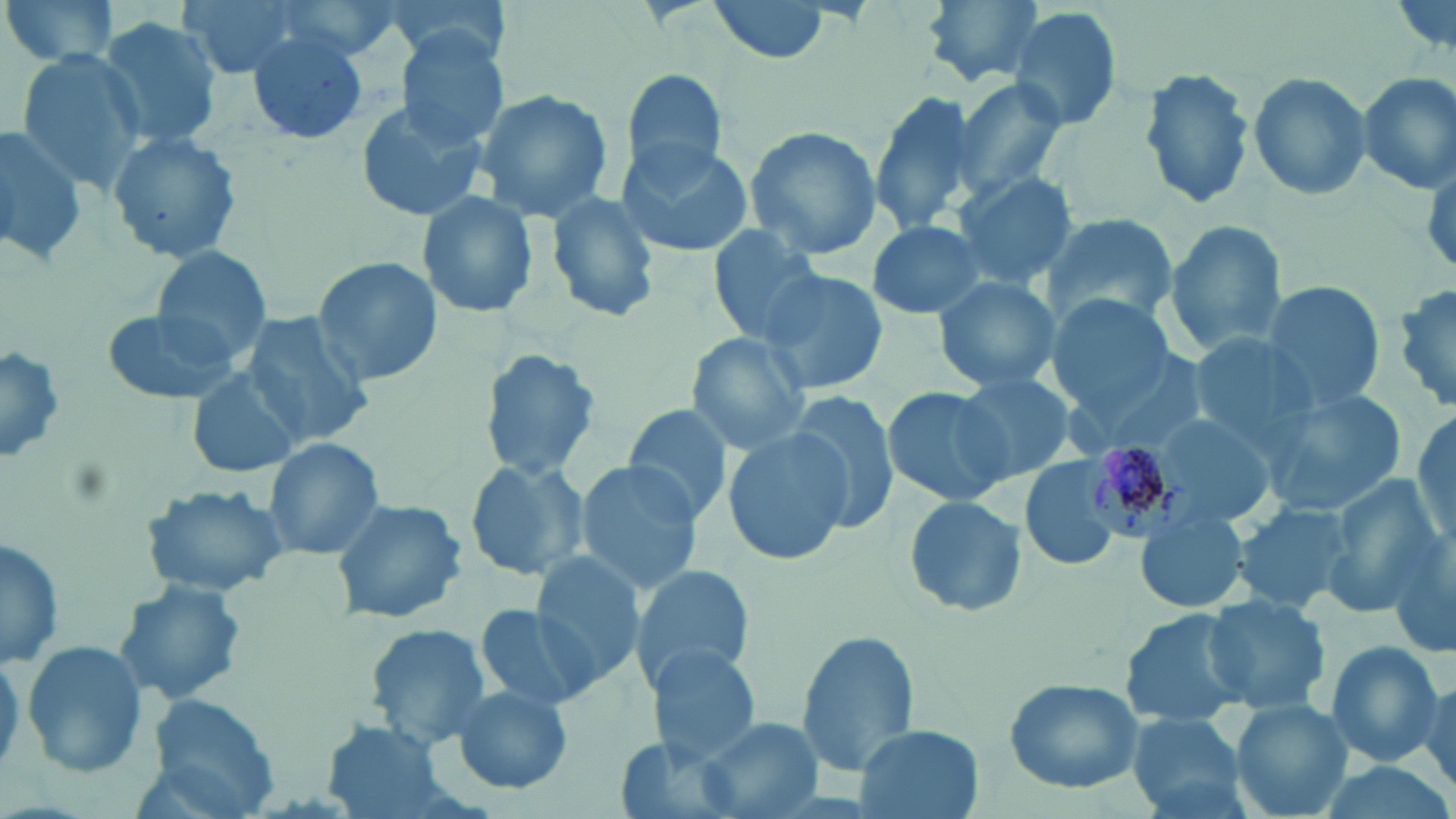 Approximate bounding boxes as named x1/y1/x2/y2 corners in pixels. Plasmodium malariae-infected red blood cell locations: (x1=1075, y1=437, x2=1194, y2=545). Uninfected red blood cell locations: (x1=1, y1=0, x2=123, y2=69), (x1=176, y1=0, x2=312, y2=78), (x1=707, y1=0, x2=832, y2=65), (x1=921, y1=0, x2=1051, y2=86), (x1=1009, y1=5, x2=1125, y2=133), (x1=99, y1=17, x2=222, y2=151), (x1=246, y1=30, x2=369, y2=147), (x1=394, y1=30, x2=509, y2=148), (x1=13, y1=49, x2=146, y2=191), (x1=1137, y1=64, x2=1259, y2=210), (x1=623, y1=68, x2=729, y2=179), (x1=1247, y1=69, x2=1372, y2=200), (x1=1356, y1=70, x2=1456, y2=193), (x1=948, y1=77, x2=1068, y2=205), (x1=471, y1=88, x2=616, y2=223), (x1=868, y1=91, x2=981, y2=234), (x1=353, y1=96, x2=486, y2=222), (x1=0, y1=124, x2=86, y2=267), (x1=742, y1=124, x2=883, y2=259), (x1=106, y1=129, x2=243, y2=265), (x1=616, y1=140, x2=756, y2=256), (x1=950, y1=171, x2=1077, y2=289), (x1=418, y1=190, x2=541, y2=320), (x1=545, y1=191, x2=661, y2=323), (x1=1041, y1=212, x2=1178, y2=327), (x1=865, y1=220, x2=990, y2=320), (x1=1164, y1=220, x2=1289, y2=358), (x1=709, y1=224, x2=832, y2=346), (x1=150, y1=246, x2=273, y2=360), (x1=313, y1=258, x2=442, y2=390), (x1=754, y1=266, x2=891, y2=399), (x1=934, y1=274, x2=1060, y2=390), (x1=1260, y1=280, x2=1386, y2=409), (x1=1391, y1=281, x2=1456, y2=416), (x1=1048, y1=294, x2=1176, y2=416), (x1=102, y1=305, x2=242, y2=407), (x1=238, y1=312, x2=374, y2=448), (x1=1184, y1=331, x2=1313, y2=439), (x1=685, y1=332, x2=812, y2=454), (x1=0, y1=342, x2=67, y2=468), (x1=477, y1=349, x2=603, y2=480), (x1=185, y1=367, x2=304, y2=480), (x1=951, y1=371, x2=1075, y2=482), (x1=882, y1=385, x2=1018, y2=508), (x1=1267, y1=390, x2=1408, y2=512), (x1=787, y1=393, x2=902, y2=532), (x1=622, y1=403, x2=737, y2=527), (x1=1411, y1=409, x2=1454, y2=547), (x1=1152, y1=411, x2=1281, y2=523), (x1=722, y1=429, x2=851, y2=566), (x1=260, y1=435, x2=386, y2=561), (x1=1019, y1=456, x2=1123, y2=571), (x1=463, y1=458, x2=589, y2=581), (x1=574, y1=461, x2=706, y2=591), (x1=1320, y1=474, x2=1446, y2=611), (x1=141, y1=482, x2=290, y2=597), (x1=329, y1=496, x2=468, y2=625), (x1=904, y1=496, x2=1026, y2=616), (x1=1231, y1=500, x2=1353, y2=613), (x1=1136, y1=508, x2=1250, y2=616), (x1=0, y1=532, x2=64, y2=670), (x1=1388, y1=534, x2=1456, y2=665), (x1=531, y1=551, x2=647, y2=688), (x1=630, y1=563, x2=754, y2=694), (x1=113, y1=577, x2=250, y2=707), (x1=1202, y1=594, x2=1331, y2=714), (x1=473, y1=603, x2=593, y2=712), (x1=1117, y1=608, x2=1252, y2=729), (x1=365, y1=624, x2=491, y2=747), (x1=795, y1=628, x2=919, y2=777), (x1=21, y1=639, x2=151, y2=776), (x1=1321, y1=640, x2=1445, y2=765), (x1=646, y1=646, x2=763, y2=763), (x1=1414, y1=673, x2=1455, y2=800), (x1=1004, y1=678, x2=1147, y2=794), (x1=447, y1=683, x2=574, y2=792), (x1=143, y1=693, x2=280, y2=816), (x1=1229, y1=699, x2=1354, y2=818), (x1=1127, y1=713, x2=1251, y2=818), (x1=694, y1=716, x2=822, y2=818), (x1=319, y1=722, x2=450, y2=816), (x1=853, y1=724, x2=984, y2=819). Slide-level diagnosis: Plasmodium malariae. 1000x magnification. May-Grünwald-Giemsa-stained preparation. Image is 1456×819 pixels. Thin blood film. Optical microscopy. One field of a larger specimen.